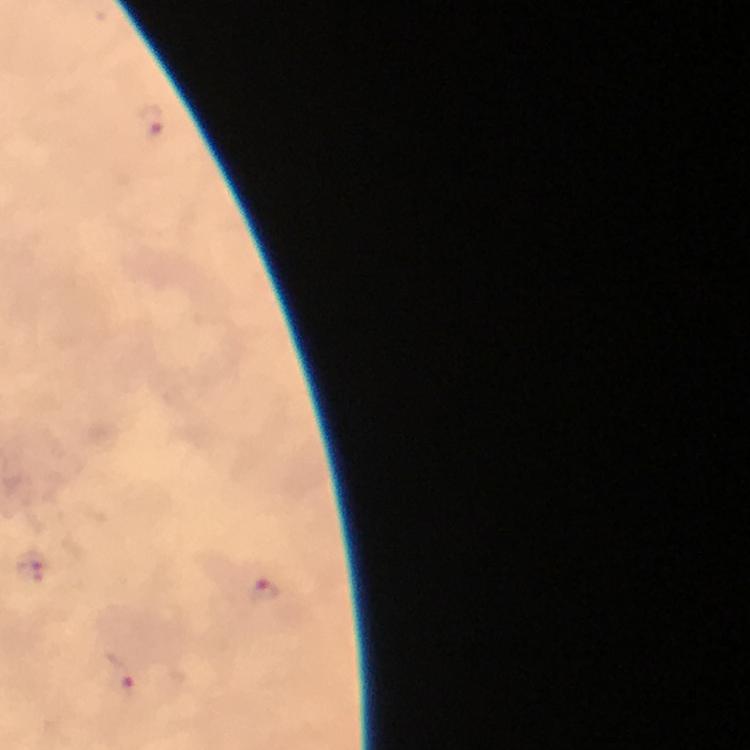

image size = 750×750 pixels
context = from a malaria diagnostic workup
stain = Giemsa
preparation = thick smear
Plasmodium parasite locations = approximate centers as {x, y} in pixels: {151, 124}, {30, 567}, {266, 591}, {117, 676}
magnification = 100x
immersion oil = used
capture = smartphone mounted on the microscope
cropped from = a single field of view